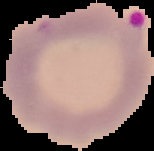
Summary:
  - Result: Plasmodium parasites detected
  - Preparation: thin blood film
  - Image type: cell region segmented out of the field of view; surrounding area masked to black
  - Image size: 154×151 pixels